Name the parasite shown.
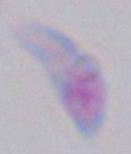
Toxoplasma gondii.

1000x magnification. Photomicrograph.